Report the malaria status of this cell.
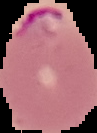

It is parasitized.

{
  "image_size": "97×133 pixels",
  "preparation": "thin blood smear",
  "image_type": "cell region segmented out of the field of view; surrounding area masked to black"
}